Name the parasite shown.
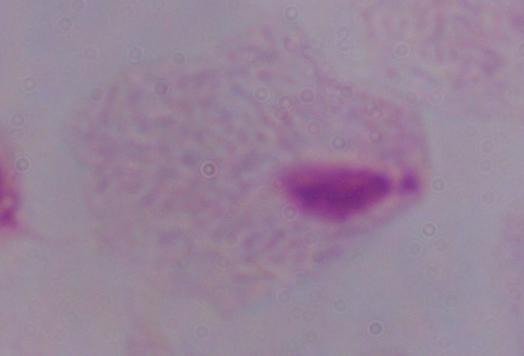

A trichomonad.

Photomicrograph. Captured at 1000x magnification.